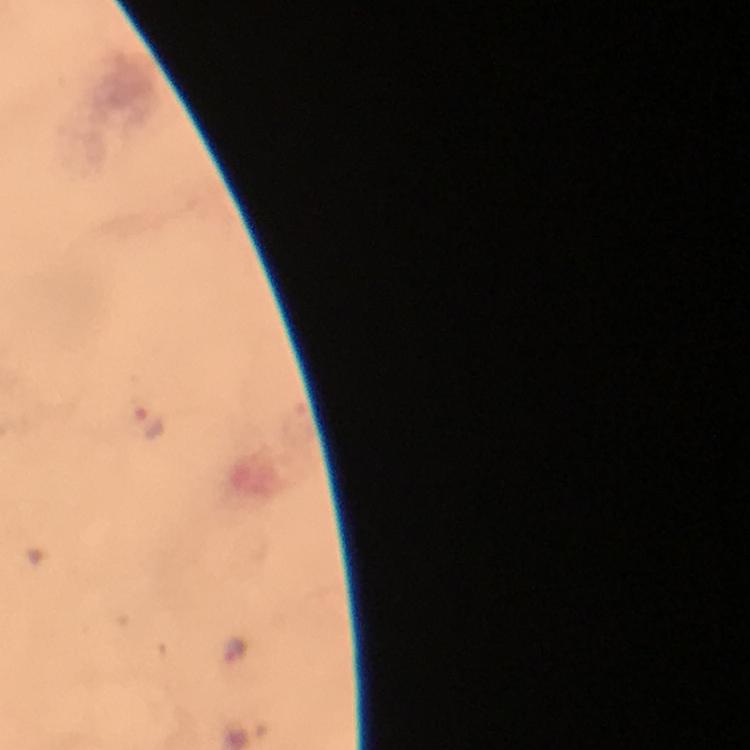
Approximate centers as [x, y] in pixels.
Summary:
  - Malaria parasite locations: [150, 422], [236, 648]
  - Magnification: 100x
  - Context: from a diagnostic examination for malaria
  - Preparation: thick blood film
  - Cropped from: a single field of view
  - Immersion oil: applied
  - Image size: 750×750 pixels
  - Stain: Giemsa
  - Capture: smartphone mounted on the microscope